Name the blood parasite species.
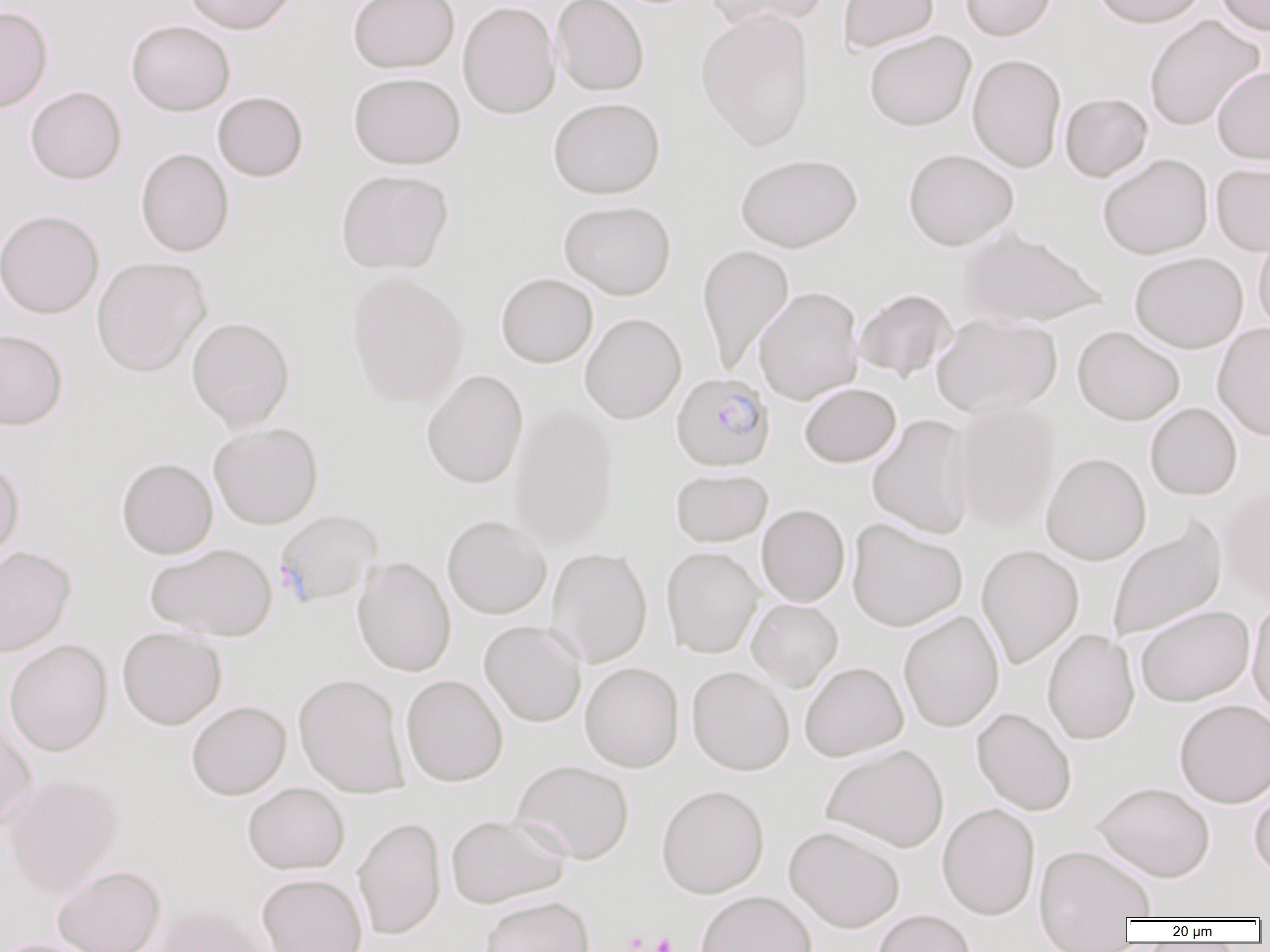
Plasmodium falciparum.

image size = 1270×952 pixels
magnification = 1000x
platelet locations = approximate bounding boxes as (x1, y1, x2, y2) in pixels: (624, 931, 648, 952), (650, 932, 677, 952)
preparation = thin blood smear
field of view = single
modality = optical microscopy
uninfected red blood cell locations = approximate bounding boxes as (x1, y1, x2, y2) in pixels: (182, 0, 299, 34), (347, 0, 459, 73), (551, 0, 649, 96), (704, 0, 830, 30), (838, 0, 939, 54), (960, 0, 1058, 41), (1090, 0, 1208, 28), (1214, 0, 1270, 35), (457, 1, 561, 119), (0, 6, 53, 113), (696, 8, 816, 151), (1144, 15, 1264, 131), (126, 20, 236, 116), (864, 30, 976, 131), (967, 54, 1067, 173), (1212, 67, 1270, 165), (348, 72, 466, 169), (25, 86, 127, 185), (213, 91, 309, 182), (1060, 93, 1152, 182), (548, 97, 665, 198), (135, 148, 234, 257), (903, 148, 1019, 251), (735, 153, 862, 252), (1098, 153, 1213, 259), (1211, 162, 1270, 255), (335, 169, 454, 274), (558, 200, 676, 299), (0, 209, 104, 319), (957, 227, 1108, 328), (1254, 228, 1270, 338), (697, 243, 795, 376), (1129, 252, 1249, 353), (91, 256, 212, 377), (346, 271, 470, 407), (496, 273, 598, 368), (753, 286, 864, 405), (853, 288, 958, 382), (580, 313, 686, 424), (930, 313, 1062, 418), (186, 316, 295, 431), (1212, 322, 1270, 441), (1072, 325, 1185, 426), (0, 329, 68, 430), (421, 369, 529, 489), (799, 382, 901, 467), (950, 401, 1059, 529), (1145, 402, 1242, 500), (509, 405, 619, 548), (866, 414, 976, 539), (208, 422, 324, 529), (1040, 451, 1151, 565), (116, 457, 218, 559), (0, 458, 24, 566), (670, 468, 773, 547), (1221, 482, 1270, 606), (756, 504, 850, 607), (442, 514, 552, 619), (1106, 515, 1227, 643), (846, 518, 967, 631), (145, 542, 277, 641), (976, 544, 1084, 669), (0, 546, 76, 657), (661, 546, 763, 658), (546, 547, 653, 667), (352, 556, 456, 677), (1247, 598, 1270, 720), (747, 599, 843, 691), (1135, 604, 1255, 707), (898, 610, 1004, 732), (479, 621, 586, 727), (117, 626, 227, 730), (1042, 628, 1140, 745), (4, 638, 113, 756), (799, 661, 909, 761), (580, 662, 684, 772), (687, 666, 794, 775), (293, 672, 410, 798), (401, 674, 508, 786), (1174, 699, 1270, 808), (186, 700, 291, 800), (972, 707, 1077, 815), (0, 718, 37, 833), (821, 743, 949, 852), (511, 759, 635, 864), (1, 773, 124, 895), (1248, 777, 1270, 880), (1092, 781, 1215, 882), (242, 782, 350, 874), (656, 784, 770, 898), (936, 802, 1041, 921), (445, 813, 570, 908), (352, 816, 446, 940), (783, 825, 905, 933), (1034, 844, 1156, 933), (52, 864, 166, 952), (257, 873, 368, 952), (695, 890, 818, 952), (478, 895, 595, 952), (150, 901, 271, 952), (872, 910, 977, 952), (0, 938, 102, 952)
Plasmodium falciparum-infected red blood cell locations = approximate bounding boxes as (x1, y1, x2, y2) in pixels: (671, 373, 775, 471), (274, 509, 382, 608)